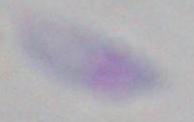

Summary:
  - Modality: micrograph
  - Magnification: 1000x
  - Identification: Toxoplasma gondii